State the blood parasite species.
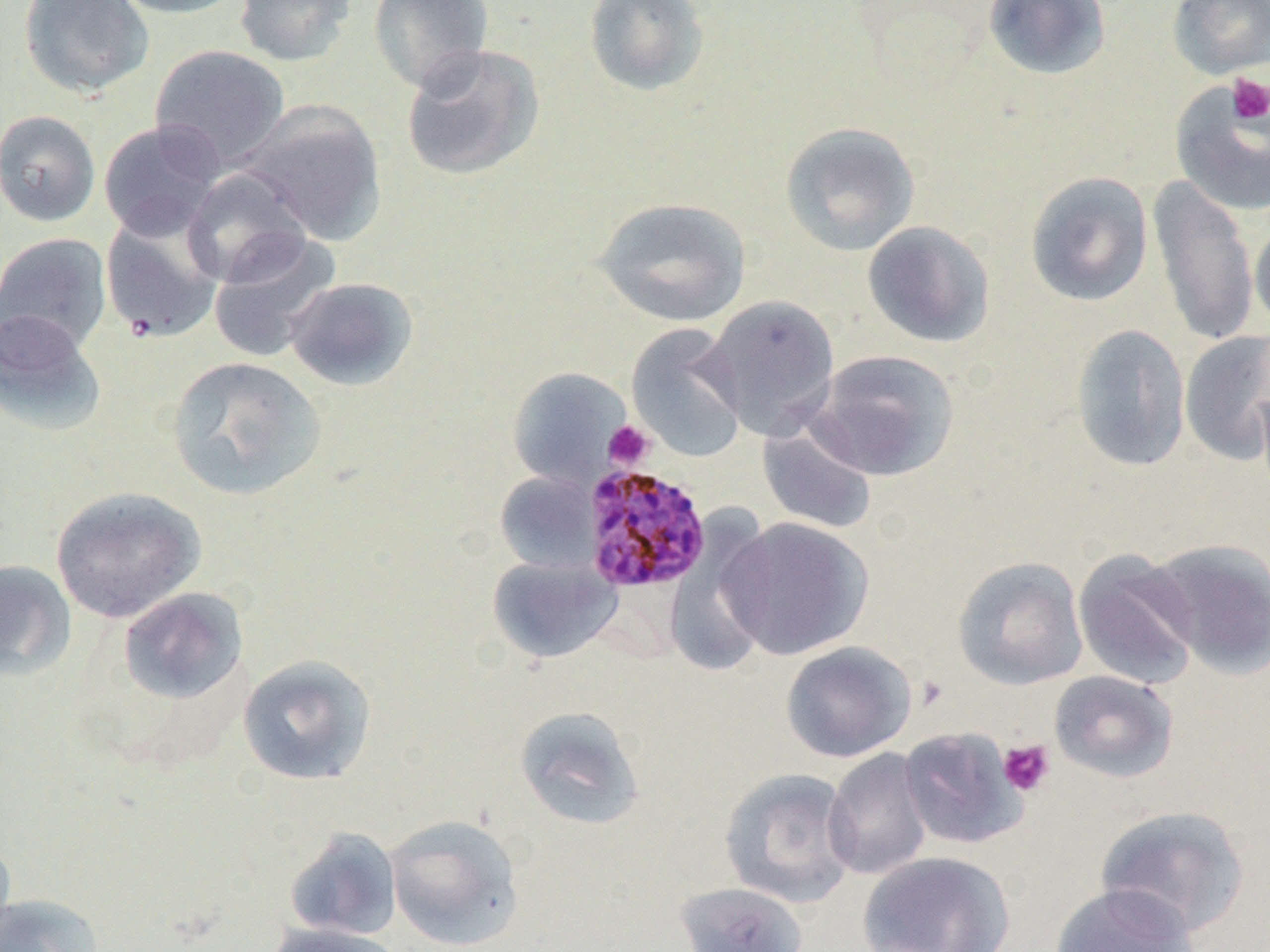

Plasmodium malariae.

Approximate bounding boxes as (x1,y1)-(x2,y2) corner pairs in pixels. Uninfected red blood cell locations: (18,0)-(154,98), (109,0)-(251,19), (233,0)-(358,66), (368,0)-(495,94), (583,0)-(711,97), (982,0)-(1112,80), (1167,0)-(1270,79), (400,43)-(545,183), (149,44)-(290,170), (1169,80)-(1270,217), (239,102)-(386,244), (0,110)-(101,227), (98,120)-(226,241), (779,121)-(921,257), (181,167)-(313,288), (1025,170)-(1154,308), (1146,174)-(1260,350), (592,197)-(751,327), (100,212)-(225,344), (1250,219)-(1270,335), (862,220)-(996,349), (207,231)-(341,363), (0,232)-(113,354), (284,276)-(419,391), (702,294)-(841,438), (0,309)-(106,436), (626,323)-(748,463), (1070,323)-(1191,472), (1179,331)-(1270,465), (808,349)-(960,481), (165,355)-(327,501), (507,367)-(633,488), (757,421)-(877,534), (495,471)-(602,575), (50,486)-(206,623), (663,512)-(778,676), (718,517)-(874,661), (1144,538)-(1270,678), (1073,549)-(1202,690), (487,555)-(623,664), (952,556)-(1088,690), (0,559)-(77,682), (117,587)-(249,704), (780,641)-(916,762), (237,654)-(377,786), (1049,670)-(1179,783), (513,705)-(645,831), (898,726)-(1027,850), (823,748)-(932,881), (719,767)-(857,907), (1095,804)-(1252,939), (384,813)-(525,950), (283,827)-(403,941), (0,833)-(17,949), (857,850)-(1016,952), (673,881)-(809,952), (1048,883)-(1200,952), (0,892)-(105,952), (264,922)-(406,952). Platelet locations: (1227,75)-(1270,125), (603,421)-(655,470), (998,739)-(1055,797). Plasmodium malariae-infected red blood cell locations: (581,463)-(711,594). Thin blood film. Optical microscopy. 1000x magnification. One field of a larger specimen. Image is 1270×952 pixels.